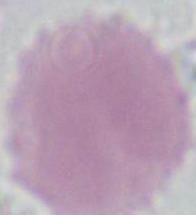
A red blood cell is seen. Micrograph. 1000x magnification.